Locate every blood parasite and identify its species.
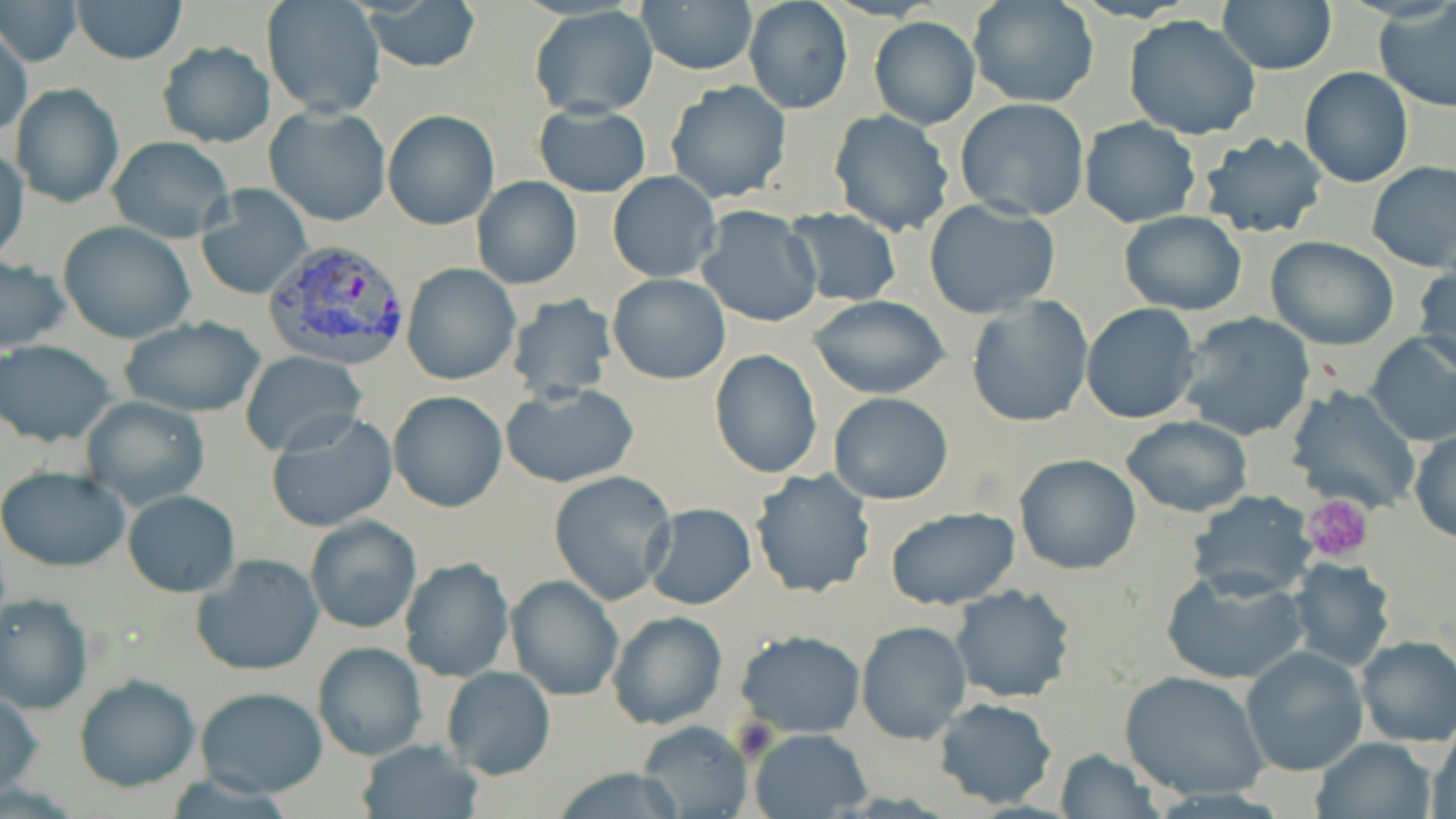

Approximate bounding boxes as (x1,y1)-(x2,y2) corner pairs in pixels.
Plasmodium vivax-infected red blood cells: (264,238)-(412,370).
No Plasmodium falciparum, Plasmodium ovale, Plasmodium malariae, Babesia divergens, or Trypanosoma brucei observed.

slide_level_diagnosis: Plasmodium vivax
image_size: 1456×819 pixels
uninfected_red_blood_cell_locations: 'approximate bounding boxes as (x1,y1)-(x2,y2) corner pairs in pixels: (1,0)-(82,66), (71,0)-(186,63), (262,0)-(386,120), (357,0)-(484,71), (743,0)-(854,115), (1217,0)-(1337,75), (638,1)-(758,76), (968,1)-(1098,109), (530,7)-(659,116), (1375,7)-(1456,114), (1121,14)-(1263,140), (869,16)-(980,129), (0,21)-(30,141), (156,40)-(274,149), (1298,68)-(1413,188), (665,81)-(793,205), (8,83)-(125,207), (954,99)-(1092,222), (533,103)-(652,197), (263,105)-(392,227), (382,108)-(500,230), (829,110)-(954,238), (1078,117)-(1201,226), (1198,132)-(1327,240), (105,136)-(235,242), (1,148)-(28,265), (1366,161)-(1456,272), (607,172)-(722,282), (472,176)-(581,289), (195,185)-(312,301), (924,199)-(1061,318), (695,205)-(823,328), (785,208)-(901,306), (1118,211)-(1246,315), (58,221)-(196,344), (1266,237)-(1399,350), (0,256)-(73,354), (401,263)-(521,386), (1414,266)-(1456,377), (607,274)-(730,385), (507,294)-(617,402), (807,295)-(952,400), (966,295)-(1092,427), (1080,303)-(1201,423), (1176,312)-(1316,441), (119,317)-(267,418), (1365,333)-(1456,446), (0,341)-(118,446), (710,348)-(822,477), (239,350)-(366,458), (499,383)-(641,489), (1285,384)-(1421,516), (388,390)-(507,513), (830,392)-(953,504), (79,395)-(212,511), (265,411)-(399,534), (1120,416)-(1252,517), (1410,430)-(1455,543), (1014,454)-(1142,574), (0,467)-(131,570), (750,468)-(876,598), (548,470)-(676,605), (122,490)-(240,597), (1190,490)-(1320,600), (643,503)-(758,610), (884,505)-(1021,610), (304,515)-(422,635), (192,554)-(325,676), (1285,557)-(1396,672), (399,558)-(517,682), (1161,571)-(1306,686), (504,574)-(625,701), (949,584)-(1076,702), (1,594)-(94,714), (608,611)-(726,730), (855,620)-(972,743), (736,630)-(865,738), (1355,636)-(1456,747), (311,641)-(428,762), (1240,646)-(1368,776), (441,666)-(556,780), (1119,670)-(1270,802), (73,674)-(200,791), (196,687)-(329,797), (1,688)-(44,797), (931,697)-(1058,808), (635,722)-(754,818), (1427,726)-(1455,819), (747,727)-(875,818), (1312,738)-(1435,819), (358,740)-(484,819), (1056,750)-(1161,819), (551,766)-(693,819)'
magnification: 1000x
platelet_locations: 'approximate bounding boxes as (x1,y1)-(x2,y2) corner pairs in pixels: (1302,496)-(1375,563)'
modality: light microscopy
field_of_view: one of a larger specimen
stain: May-Grünwald-Giemsa
preparation: thin blood smear